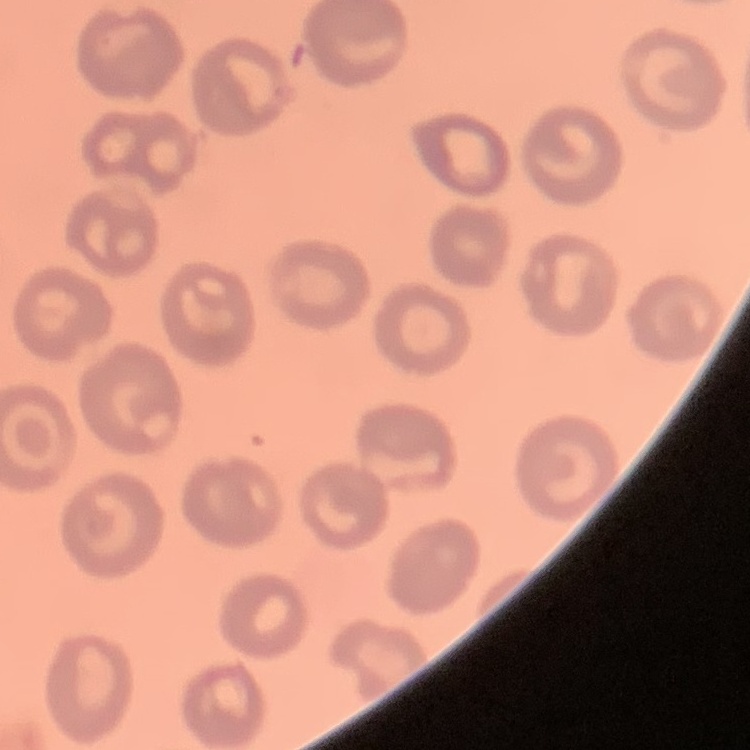

red blood cell morphology = no rouleaux formation
stain = Field's or Giemsa
preparation = thin blood film
image type = one tile cut from a larger photomicrograph